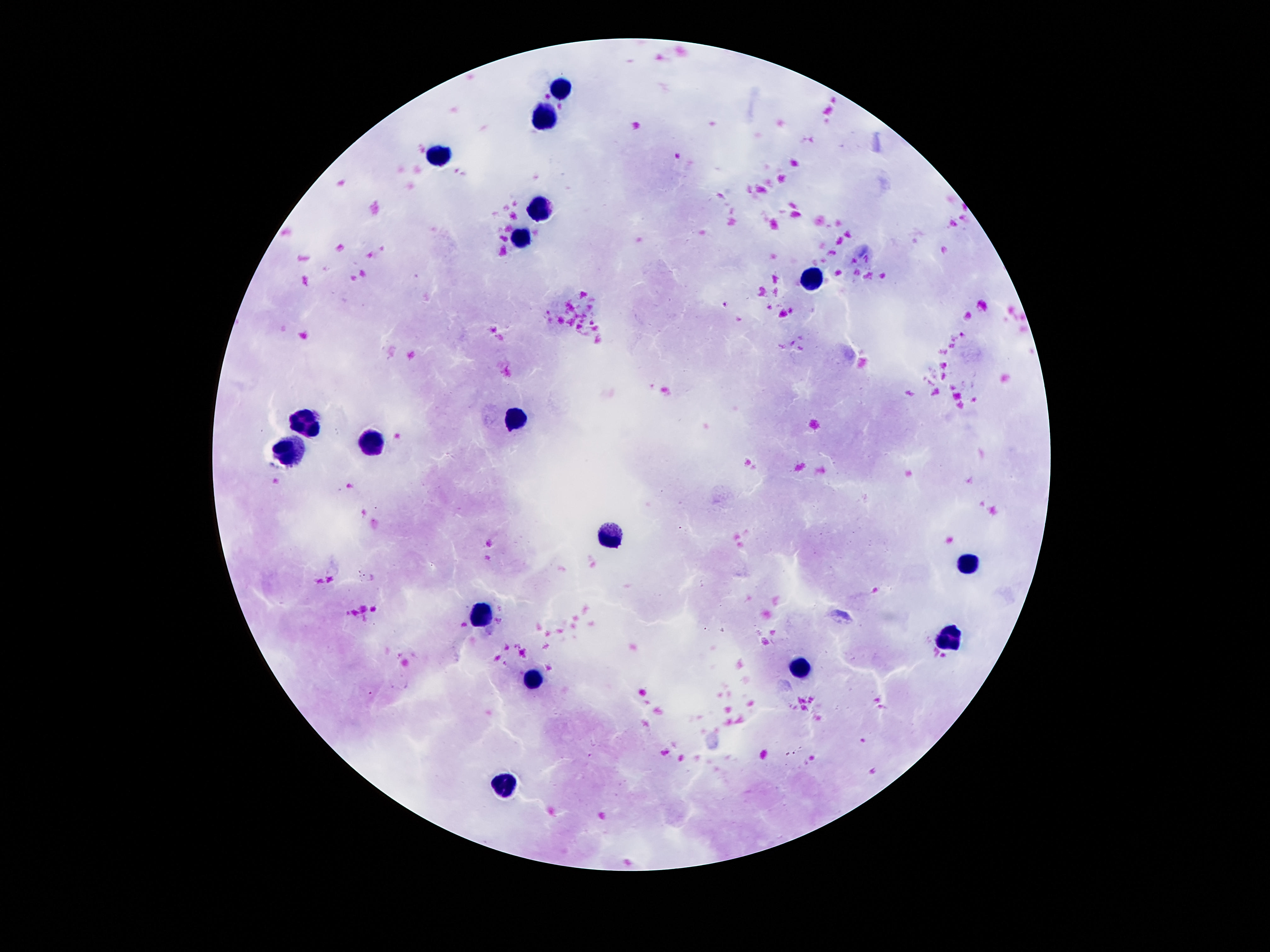
Approximate centers as {x, y} in pixels. Leukocyte locations: {563, 87}, {542, 116}, {439, 155}, {539, 207}, {521, 240}, {808, 278}, {518, 421}, {304, 425}, {371, 445}, {292, 450}, {611, 536}, {970, 566}, {481, 612}, {951, 641}, {802, 667}, {531, 677}, {502, 787}. Single field of view. Patient malaria status: uninfected. 100x magnification. Image is 1270×952 pixels. Thick peripheral-blood smear. Giemsa-stained preparation. Photographed through the microscope eyepiece with a smartphone camera.